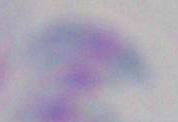 1000x magnification. Toxoplasma gondii is seen. Micrograph.